Comment on the morphology of the red blood cells.
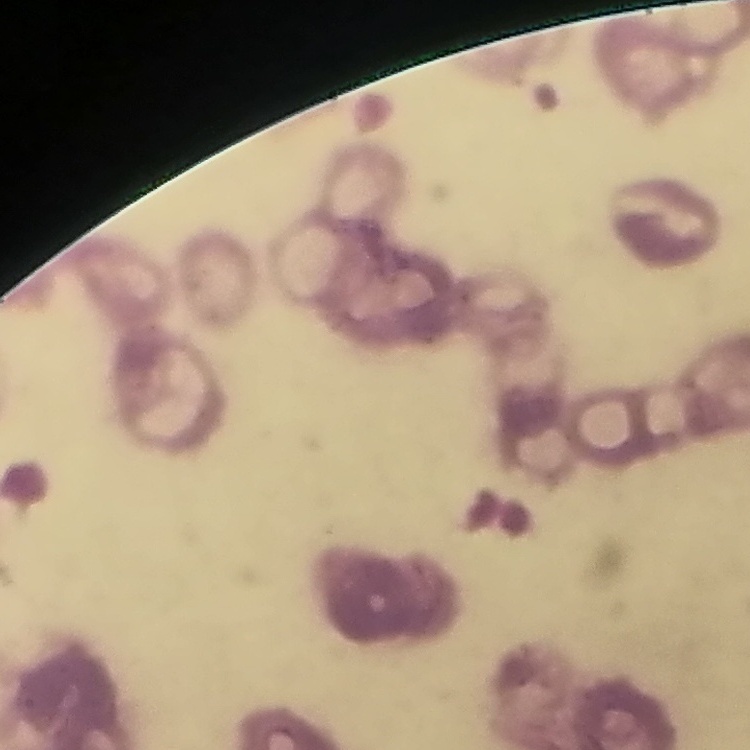

Rouleaux formation.

Summary:
  - Image type: one tile cut from a larger photomicrograph
  - Preparation: thin blood smear
  - Stain: Field's or Giemsa